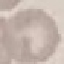

Malaria status: uninfected. Automatically extracted cell patch, resized to 64 × 64 pixels. Giemsa stain. Thin blood smear. Photographed with a smartphone camera at the microscope eyepiece.